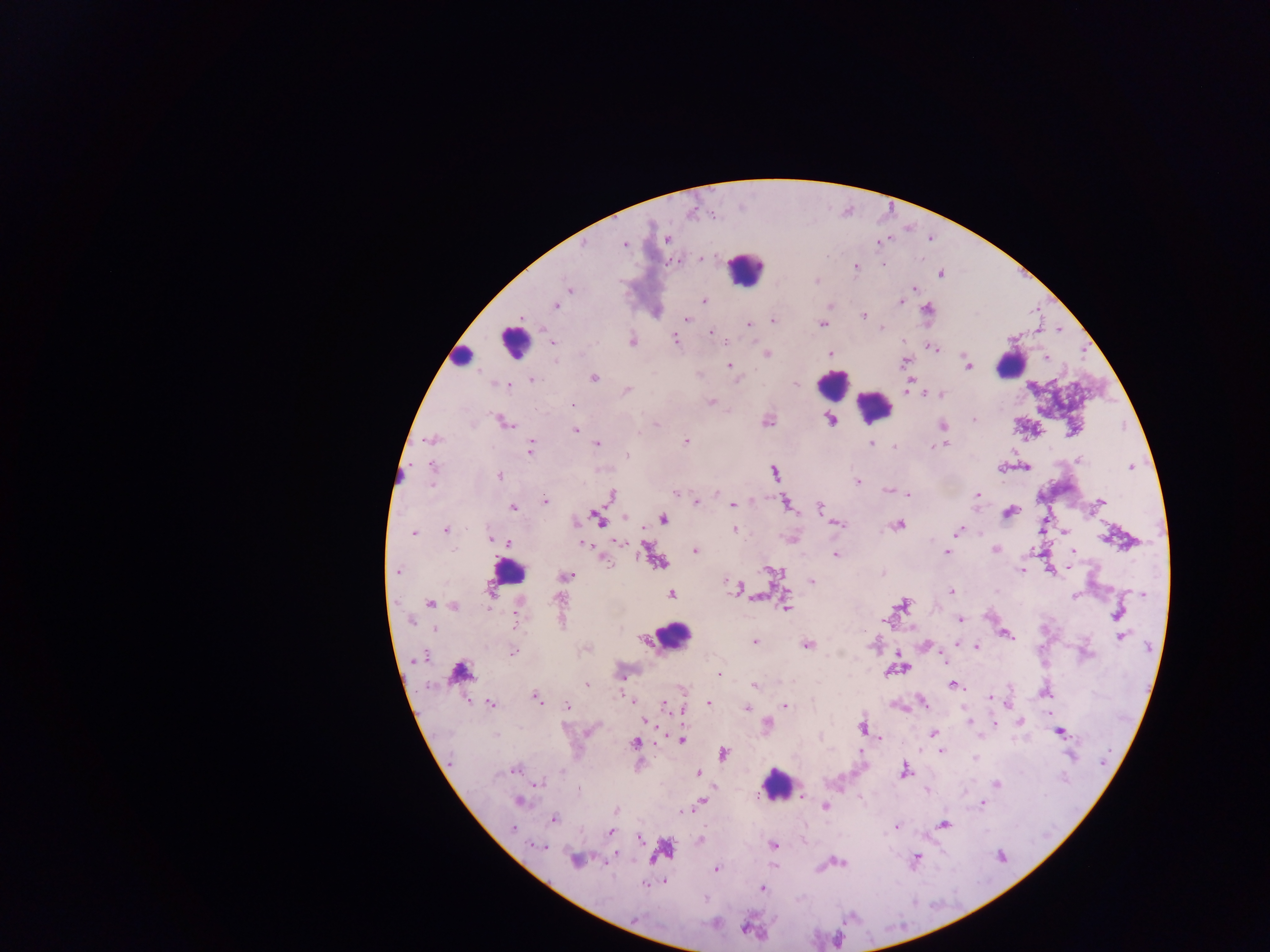
Approximate centers as x y in pixels.
Summary:
  - Malaria parasite locations: 667 240; 624 244; 702 259; 883 264; 855 266; 940 274; 816 281; 915 288; 570 289; 918 292; 704 301; 900 302; 556 306; 927 309; 863 316; 687 319; 774 321; 748 324; 823 324; 882 328; 710 332; 675 340; 553 342; 632 342; 725 342; 932 348; 830 353; 766 354; 1045 357; 904 361; 730 366; 969 366; 593 377; 532 380; 910 381; 796 384; 505 385; 909 387; 627 390; 940 395; 711 402; 573 405; 829 420; 974 420; 767 421; 504 422; 656 425; 942 426; 575 430; 431 439; 686 442; 598 443; 871 443; 935 445; 894 446; 530 449; 627 455; 1079 461; 432 467; 1026 467; 1130 467; 775 473; 499 475; 858 482; 431 487; 886 490; 717 492; 675 493; 908 494; 977 495; 612 496; 545 500; 1101 502; 697 503; 786 503; 733 505; 513 508; 820 508; 1010 511; 624 517; 598 518; 663 518; 577 521; 837 524; 899 525; 734 528; 445 530; 958 531; 1064 532; 413 533; 489 538; 582 541; 618 542; 508 543; 586 545; 455 548; 995 549; 695 550; 1073 551; 947 553; 836 555; 656 562; 606 563; 1068 567; 1020 570; 772 571; 397 573; 883 573; 566 577; 812 581; 727 582; 738 589; 951 591; 491 593; 671 594; 1142 595; 1074 596; 756 597; 558 599; 430 603; 786 605; 902 605; 455 606; 1118 614; 960 619; 516 620; 411 621; 434 630; 1007 634; 1120 637; 754 642; 958 644; 808 645; 976 647; 512 653; 422 658; 902 669; 719 674; 587 684; 753 685; 952 685; 684 690; 1046 694; 536 697; 991 697; 630 700; 709 703; 923 703; 490 704; 567 706; 664 706; 785 706; 747 708; 682 710; 970 720; 647 721; 1020 722; 767 723; 994 724; 862 727; 1059 732; 933 733; 497 735; 879 739; 681 740; 635 743; 941 751; 724 753; 975 759; 515 769; 563 770; 904 771; 699 773; 538 784; 997 785; 803 794; 519 800; 701 801; 983 803; 825 807; 617 811; 683 811; 554 819; 943 825; 895 827; 512 828; 610 832; 640 839; 700 840; 774 845; 537 846; 917 858; 575 860; 839 863; 607 864; 716 869; 664 881; 646 883; 762 889
  - Leukocyte locations: 745 268; 513 341; 461 357; 1011 365; 831 384; 875 407; 507 571; 672 635; 457 672; 777 785
  - Preparation: thick blood smear
  - Image size: 1270×952 pixels
  - Capture: mobile-phone photograph through a microscope
  - Country: Ghana
  - Field of view: single